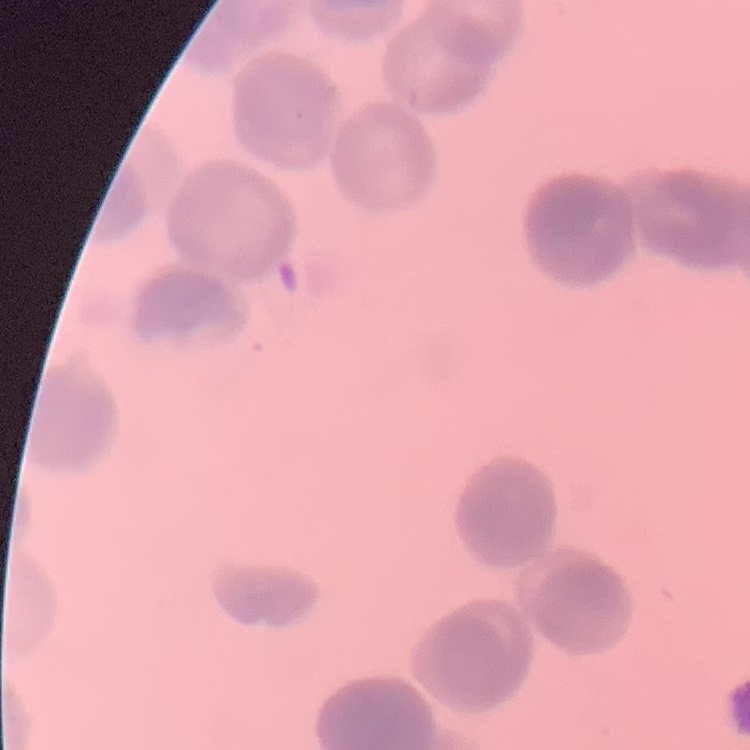
Summary:
  - Red blood cell morphology: rouleaux formation
  - Image type: square crop of a larger photomicrograph
  - Preparation: thin blood smear
  - Stain: Field's or Giemsa